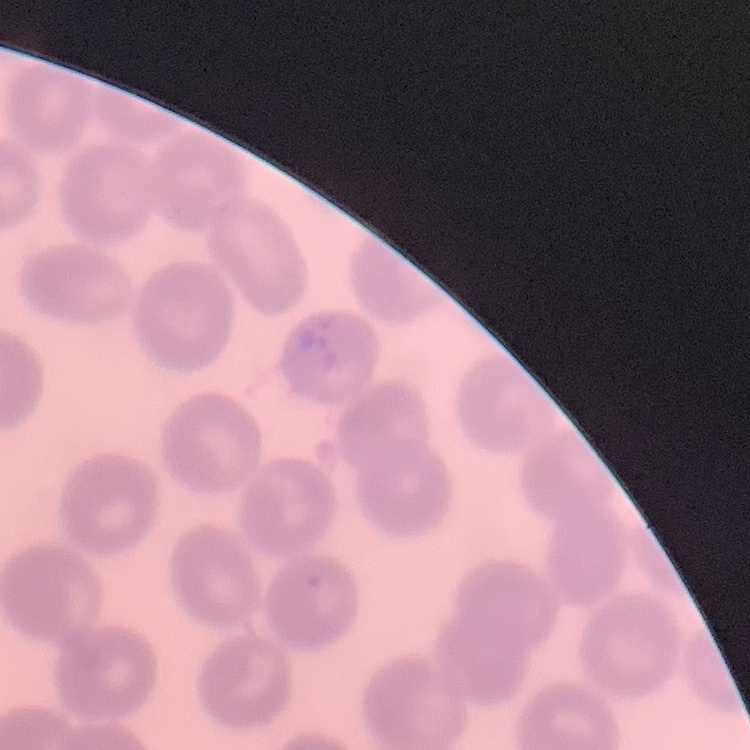

red blood cell morphology = no rouleaux formation
preparation = thin blood film
image type = square crop of a larger photomicrograph
stain = Field's or Giemsa